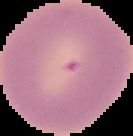
The area outside the segmented cell region is set to black. Image is 133×136 pixels. Result: negative for Plasmodium parasites. From a thin blood film.